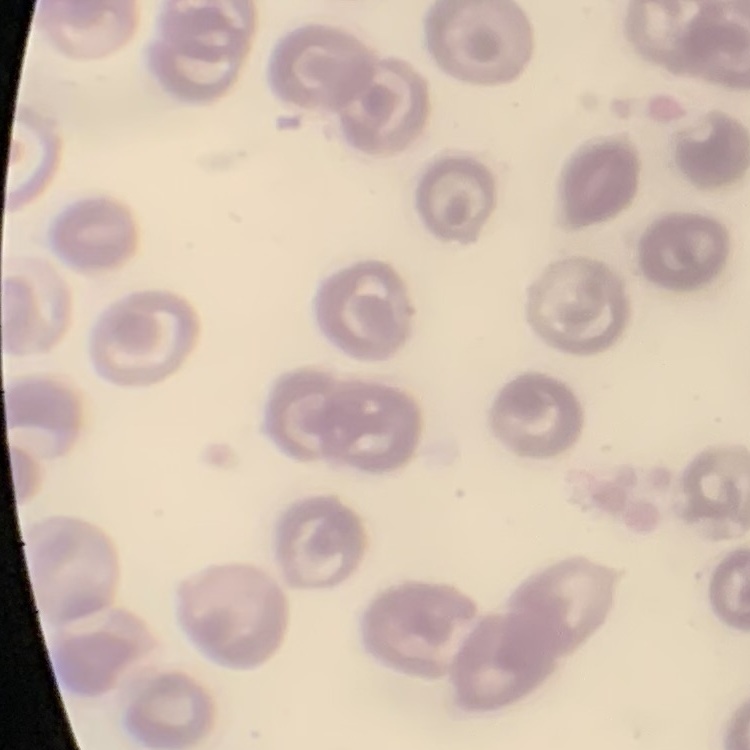
The red blood cells exhibit no rouleaux formation. Thin blood smear. Stained with either Field's or Giemsa. Square crop of a larger photomicrograph.